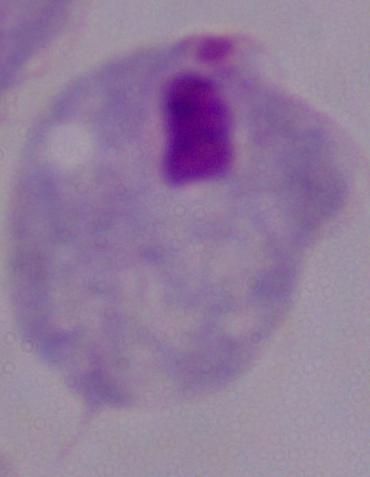
Summary:
  - Modality: micrograph
  - Identification: trichomonad
  - Magnification: 1000x